Find each parasitized red blood cell.
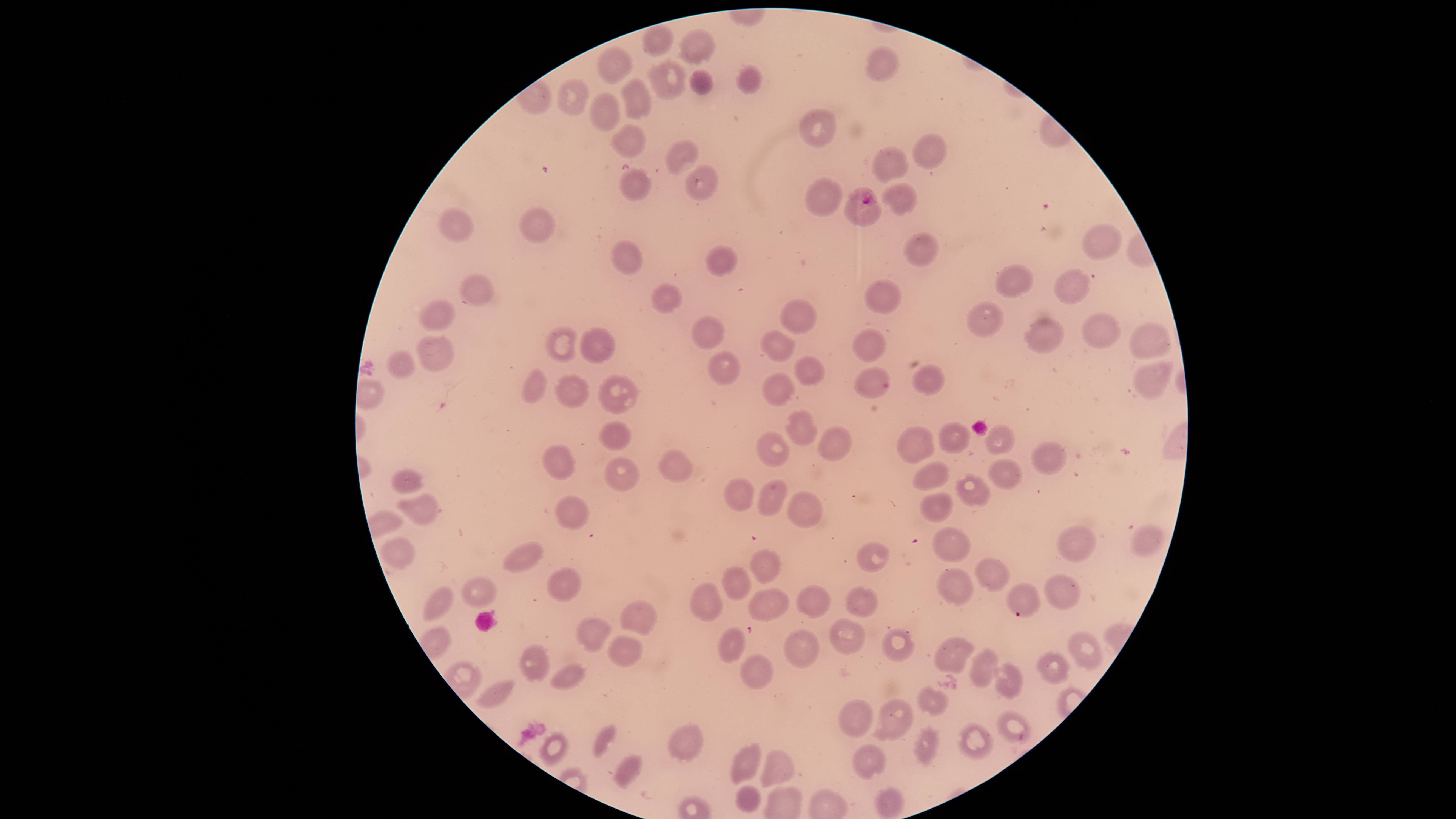

Approximate bounding boxes, in pixels from the top-left corner.
Parasitized red blood cells: (left=843, top=187, right=882, bottom=226).

Approximate bounding boxes, in pixels from the top-left corner.
Summary:
  - Uninfected red blood cells: (left=643, top=23, right=675, bottom=57), (left=679, top=30, right=714, bottom=63), (left=866, top=45, right=899, bottom=82), (left=597, top=46, right=633, bottom=84), (left=650, top=60, right=686, bottom=100), (left=738, top=66, right=762, bottom=93), (left=690, top=70, right=713, bottom=95), (left=621, top=78, right=652, bottom=120), (left=558, top=80, right=591, bottom=115), (left=590, top=93, right=620, bottom=132), (left=800, top=107, right=838, bottom=147), (left=612, top=124, right=646, bottom=159), (left=912, top=134, right=947, bottom=169), (left=666, top=140, right=699, bottom=174), (left=871, top=146, right=909, bottom=183), (left=685, top=164, right=718, bottom=200), (left=619, top=168, right=651, bottom=201), (left=804, top=178, right=843, bottom=216), (left=882, top=183, right=916, bottom=215), (left=437, top=207, right=474, bottom=241), (left=518, top=207, right=556, bottom=244), (left=1082, top=224, right=1122, bottom=259), (left=903, top=233, right=939, bottom=267), (left=611, top=239, right=644, bottom=275), (left=705, top=245, right=738, bottom=276), (left=996, top=265, right=1033, bottom=298), (left=1054, top=269, right=1091, bottom=304), (left=460, top=273, right=494, bottom=307), (left=864, top=279, right=903, bottom=314), (left=652, top=283, right=684, bottom=314), (left=419, top=297, right=456, bottom=331), (left=780, top=298, right=817, bottom=334), (left=967, top=302, right=1004, bottom=337), (left=1082, top=312, right=1122, bottom=348), (left=691, top=315, right=725, bottom=349), (left=1023, top=317, right=1067, bottom=353), (left=1129, top=321, right=1172, bottom=359), (left=545, top=326, right=581, bottom=362), (left=580, top=327, right=615, bottom=363), (left=853, top=328, right=886, bottom=362), (left=761, top=329, right=795, bottom=362), (left=416, top=336, right=454, bottom=372), (left=387, top=350, right=416, bottom=379), (left=709, top=351, right=742, bottom=385), (left=794, top=355, right=825, bottom=384), (left=1133, top=360, right=1174, bottom=399), (left=913, top=365, right=945, bottom=395), (left=855, top=366, right=892, bottom=398), (left=523, top=368, right=547, bottom=404), (left=763, top=372, right=796, bottom=407), (left=598, top=374, right=637, bottom=414), (left=557, top=375, right=589, bottom=408), (left=785, top=408, right=817, bottom=446), (left=599, top=420, right=632, bottom=450), (left=939, top=422, right=972, bottom=454), (left=986, top=424, right=1015, bottom=455), (left=896, top=425, right=936, bottom=464), (left=818, top=426, right=851, bottom=461), (left=757, top=431, right=790, bottom=468), (left=1031, top=440, right=1067, bottom=475), (left=541, top=444, right=574, bottom=479), (left=658, top=448, right=692, bottom=483), (left=604, top=456, right=640, bottom=492), (left=989, top=459, right=1022, bottom=490), (left=913, top=461, right=950, bottom=491), (left=392, top=467, right=422, bottom=494), (left=955, top=474, right=991, bottom=506), (left=724, top=476, right=756, bottom=511), (left=758, top=479, right=788, bottom=517), (left=786, top=491, right=824, bottom=529), (left=918, top=491, right=953, bottom=522), (left=395, top=492, right=439, bottom=525), (left=556, top=494, right=589, bottom=528), (left=1132, top=524, right=1164, bottom=558), (left=1056, top=525, right=1097, bottom=562), (left=932, top=527, right=971, bottom=563), (left=379, top=537, right=414, bottom=567), (left=503, top=542, right=543, bottom=572), (left=856, top=542, right=890, bottom=573), (left=751, top=549, right=780, bottom=584), (left=976, top=557, right=1010, bottom=593), (left=722, top=566, right=750, bottom=600), (left=546, top=568, right=582, bottom=602), (left=937, top=568, right=973, bottom=606), (left=1045, top=574, right=1081, bottom=610), (left=460, top=576, right=496, bottom=607), (left=690, top=582, right=724, bottom=622), (left=1006, top=582, right=1041, bottom=617), (left=422, top=584, right=454, bottom=621), (left=795, top=586, right=831, bottom=619), (left=845, top=586, right=880, bottom=618), (left=748, top=587, right=790, bottom=621), (left=621, top=599, right=658, bottom=638), (left=577, top=617, right=612, bottom=652), (left=829, top=617, right=866, bottom=655), (left=717, top=625, right=746, bottom=665), (left=785, top=628, right=819, bottom=669), (left=881, top=628, right=917, bottom=663), (left=1068, top=631, right=1102, bottom=669), (left=608, top=633, right=643, bottom=666), (left=934, top=637, right=976, bottom=674), (left=520, top=644, right=550, bottom=682), (left=968, top=649, right=998, bottom=688), (left=1038, top=651, right=1070, bottom=684), (left=741, top=653, right=774, bottom=690), (left=551, top=662, right=585, bottom=690), (left=994, top=662, right=1021, bottom=698), (left=478, top=680, right=514, bottom=708), (left=918, top=686, right=948, bottom=716), (left=838, top=699, right=874, bottom=740), (left=867, top=700, right=913, bottom=741), (left=996, top=710, right=1032, bottom=744), (left=669, top=723, right=701, bottom=761), (left=958, top=723, right=994, bottom=760), (left=594, top=724, right=616, bottom=757), (left=913, top=727, right=938, bottom=765), (left=541, top=732, right=569, bottom=765), (left=731, top=743, right=762, bottom=786), (left=851, top=744, right=885, bottom=779), (left=756, top=750, right=793, bottom=786), (left=614, top=754, right=642, bottom=786), (left=735, top=786, right=761, bottom=811), (left=875, top=787, right=907, bottom=819)
  - Stain: Giemsa
  - Field of view: single
  - Preparation: thin blood smear
  - Visible region: circular
  - Species: Plasmodium falciparum
  - Capture: smartphone photograph through the microscope eyepiece
  - Image size: 1456×819 pixels